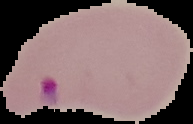
Summary:
  - Malaria status: parasitized
  - Image type: segmented cell region on a black background
  - Image size: 193×124 pixels
  - Preparation: thin blood film